Evaluate for malaria.
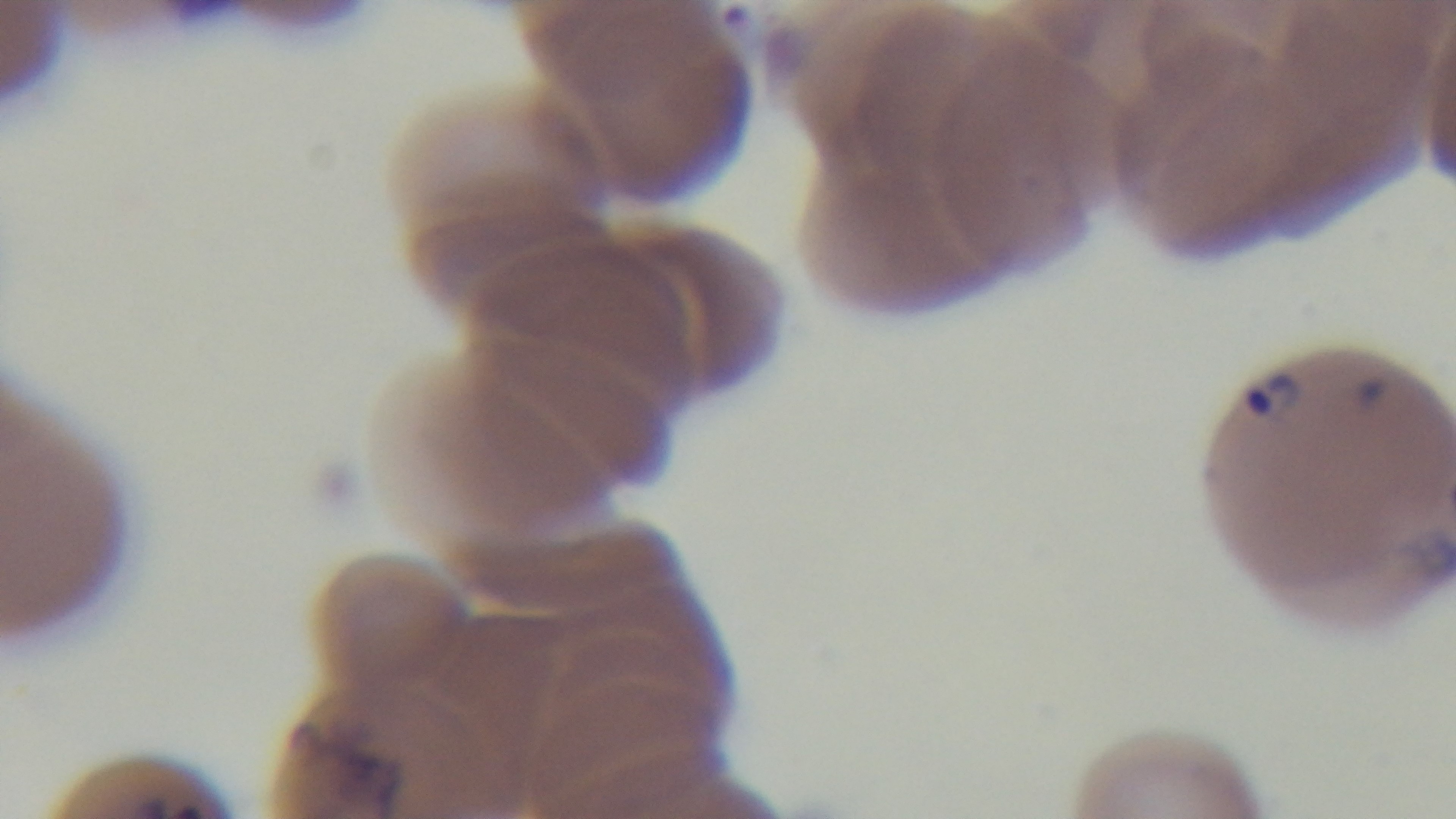
It is infected.

Summary:
  - Capture: mounted 4K digital camera
  - Modality: light microscopy
  - Field of view: single
  - Stain: Giemsa
  - Preparation: thin
  - Objective: 100x oil immersion